Classify this cell by malaria status.
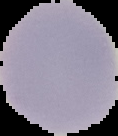
Uninfected.

Summary:
  - Preparation: thin blood film
  - Image type: segmented cell region with the area outside set to black
  - Image size: 118×136 pixels